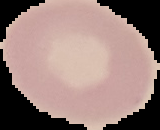
Summary:
  - Image size: 160×130 pixels
  - Result: no Plasmodium parasites seen
  - Preparation: thin blood smear
  - Image type: segmented cell region on a black background